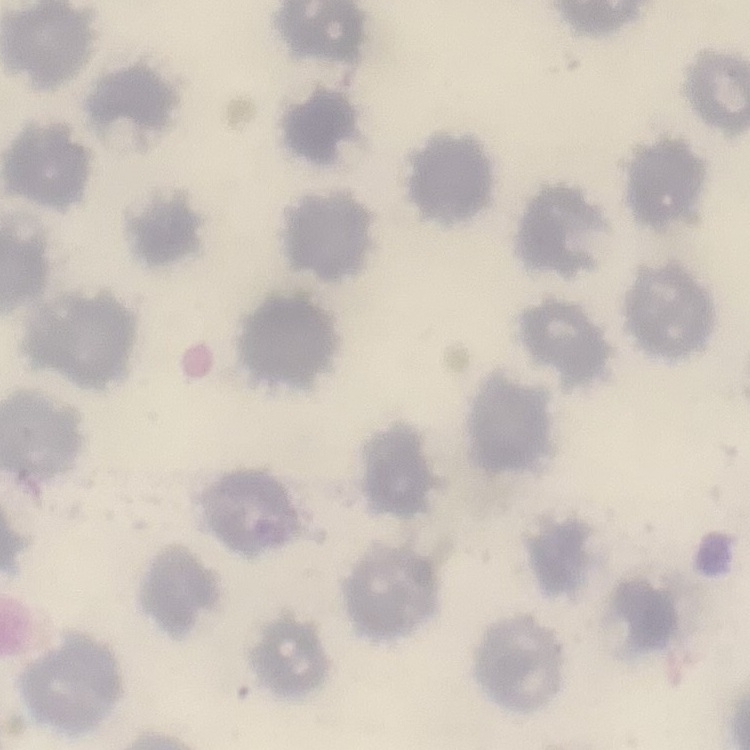
Summary:
  - Red blood cell morphology: no rouleaux formation
  - Image type: square crop of a larger photomicrograph
  - Preparation: thin blood smear
  - Stain: Field's or Giemsa